Point out each malaria parasite.
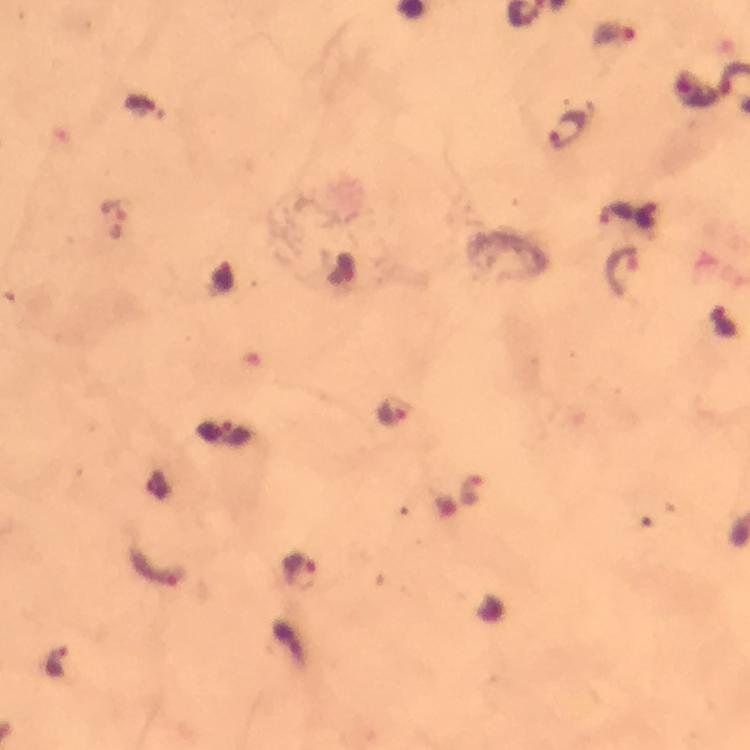
Approximate centers as {x, y} in pixels.
Malaria parasites: {615, 32}, {569, 130}, {113, 217}, {625, 271}, {394, 412}, {470, 489}, {152, 567}, {300, 571}, {56, 661}.

context = from a malaria diagnostic workup
cropped from = one field of view
image size = 750×750 pixels
preparation = thick smear
magnification = 100x
capture = smartphone camera through the microscope
immersion oil = applied
stain = Giemsa